Locate every blood parasite and identify its species.
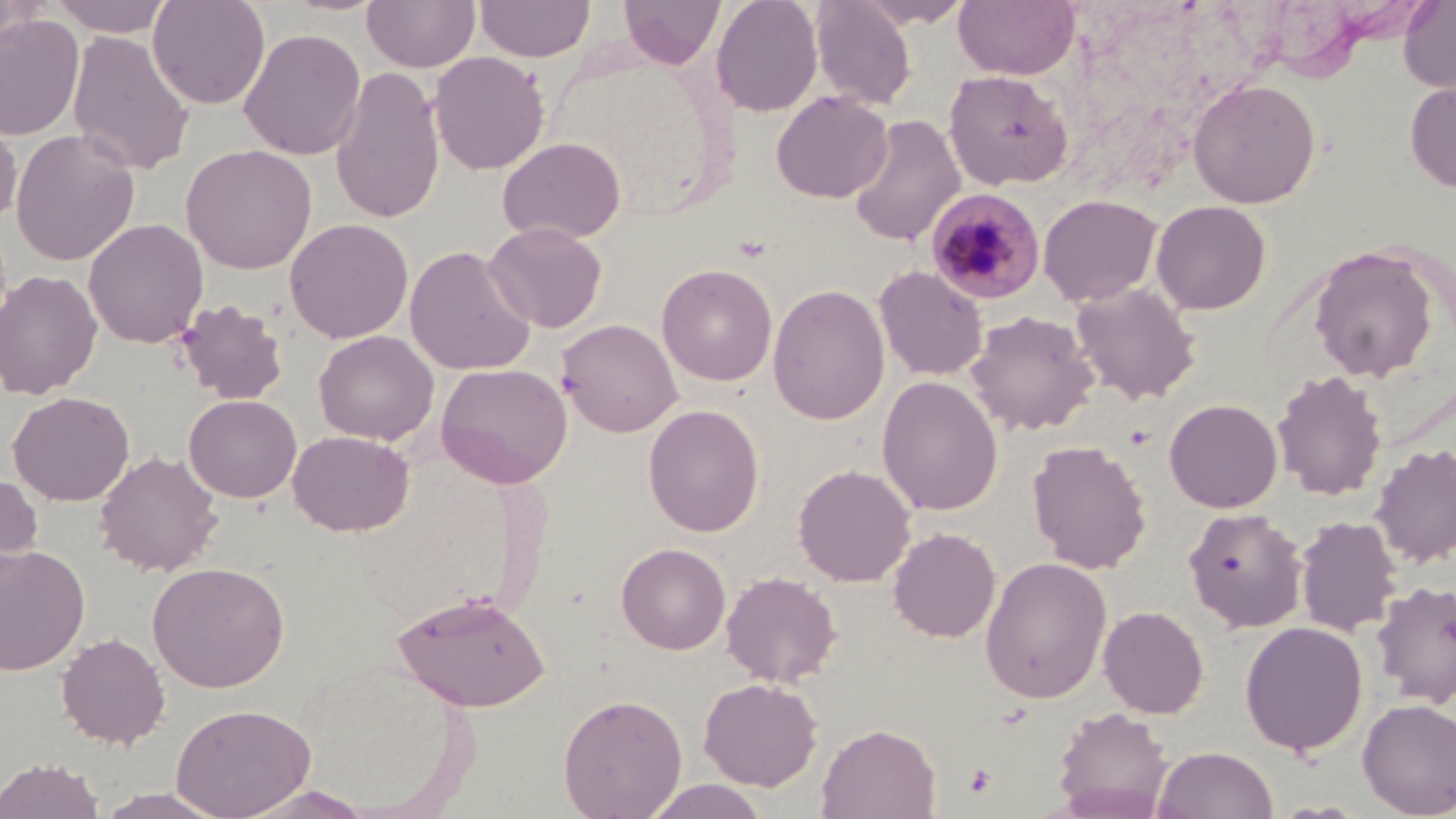

Approximate bounding boxes as [x1, y1, x2, y2] in pixels.
Plasmodium malariae-infected red blood cells: [926, 189, 1047, 305].
No Plasmodium falciparum, Plasmodium ovale, Plasmodium vivax, Babesia divergens, or Trypanosoma brucei observed.

Summary:
  - Uninfected red blood cell locations: [49, 0, 176, 37], [147, 0, 271, 110], [362, 0, 481, 72], [474, 0, 595, 62], [618, 0, 725, 68], [710, 0, 823, 118], [809, 0, 917, 109], [857, 0, 973, 28], [953, 0, 1080, 80], [1398, 0, 1456, 94], [0, 1, 48, 61], [0, 13, 84, 141], [238, 28, 366, 160], [67, 29, 196, 176], [539, 47, 729, 217], [428, 51, 550, 176], [330, 66, 445, 225], [944, 70, 1073, 190], [1187, 78, 1321, 208], [1405, 79, 1456, 194], [771, 90, 893, 204], [847, 114, 966, 248], [0, 116, 21, 230], [10, 128, 140, 266], [497, 137, 626, 244], [181, 144, 318, 274], [1037, 194, 1163, 307], [1048, 195, 1188, 395], [1151, 200, 1272, 315], [83, 218, 208, 349], [284, 218, 413, 344], [483, 222, 607, 333], [405, 245, 536, 376], [1309, 245, 1439, 382], [656, 263, 778, 386], [873, 265, 988, 381], [0, 269, 103, 399], [1070, 282, 1201, 405], [768, 283, 890, 425], [174, 298, 290, 405], [966, 310, 1099, 436], [556, 318, 682, 437], [313, 330, 439, 445], [436, 362, 573, 488], [1272, 369, 1387, 502], [877, 376, 1003, 515], [8, 390, 134, 506], [184, 394, 302, 503], [1164, 398, 1283, 513], [643, 404, 765, 537], [288, 430, 414, 536], [1027, 439, 1152, 574], [1370, 443, 1456, 569], [94, 450, 223, 577], [792, 463, 915, 587], [0, 469, 43, 584], [1183, 508, 1308, 633], [1295, 515, 1401, 637], [887, 527, 1001, 643], [615, 542, 730, 655], [0, 544, 91, 675], [979, 556, 1113, 703], [147, 561, 291, 692], [721, 571, 843, 688], [1371, 580, 1456, 707], [392, 589, 551, 711], [1098, 605, 1209, 718], [1240, 621, 1368, 755], [56, 632, 170, 749], [699, 677, 823, 791], [557, 693, 687, 819], [1357, 698, 1456, 817], [170, 703, 316, 818], [1052, 706, 1174, 816], [817, 723, 942, 818], [1152, 746, 1278, 819], [0, 756, 104, 819], [642, 779, 770, 819], [239, 784, 378, 819], [92, 788, 233, 818]
  - Platelet locations: [964, 763, 998, 799]
  - Slide-level diagnosis: Plasmodium malariae
  - Magnification: 1000x
  - Image size: 1456×819 pixels
  - Preparation: thin blood film
  - Stain: May-Grünwald-Giemsa
  - Modality: light microscopy
  - Field of view: one of a larger specimen